Look for Plasmodium parasites.
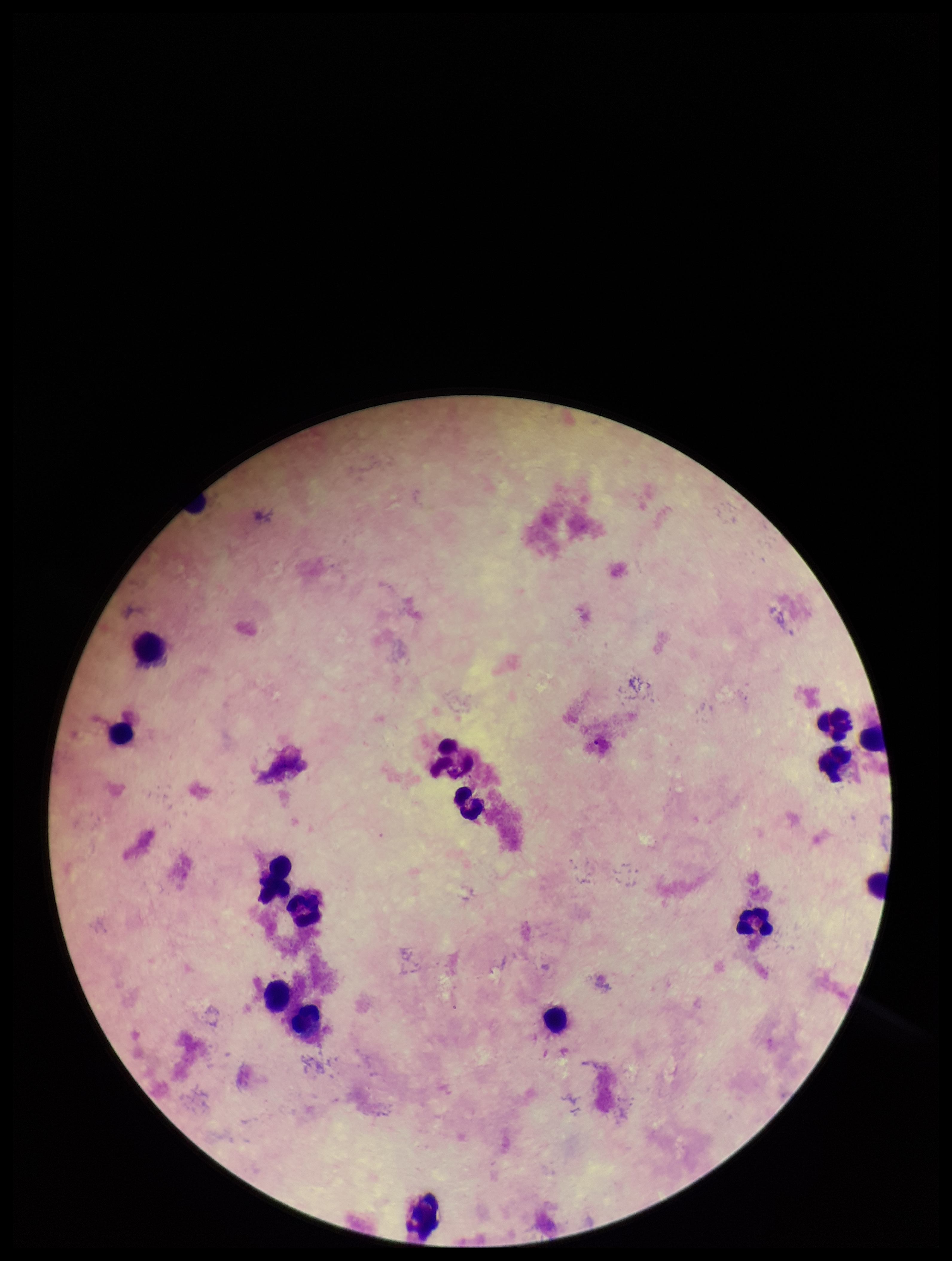
None detected.

Image is 952×1261 pixels. Patient malaria status: negative. Parasite count: 0. Giemsa stain. Leukocyte count: 16. Preparation: thick blood smear. One field from this slide. Photographed through the microscope eyepiece with a smartphone camera.